Report the malaria status of this cell.
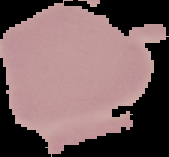
Uninfected.

image_type: cell region segmented out of the field of view; surrounding area masked to black
image_size: 169×157 pixels
preparation: thin blood film